Report the malaria status of this cell.
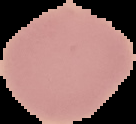
It is uninfected.

Cell region segmented out of the field of view; the surrounding area is masked to black. Image is 136×124 pixels. From a thin blood film.